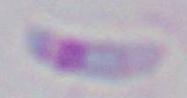
Toxoplasma gondii is seen. Micrograph. 1000x magnification.